Identify the parasite.
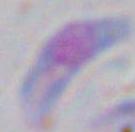

Toxoplasma gondii.

magnification: 1000x
modality: photomicrograph